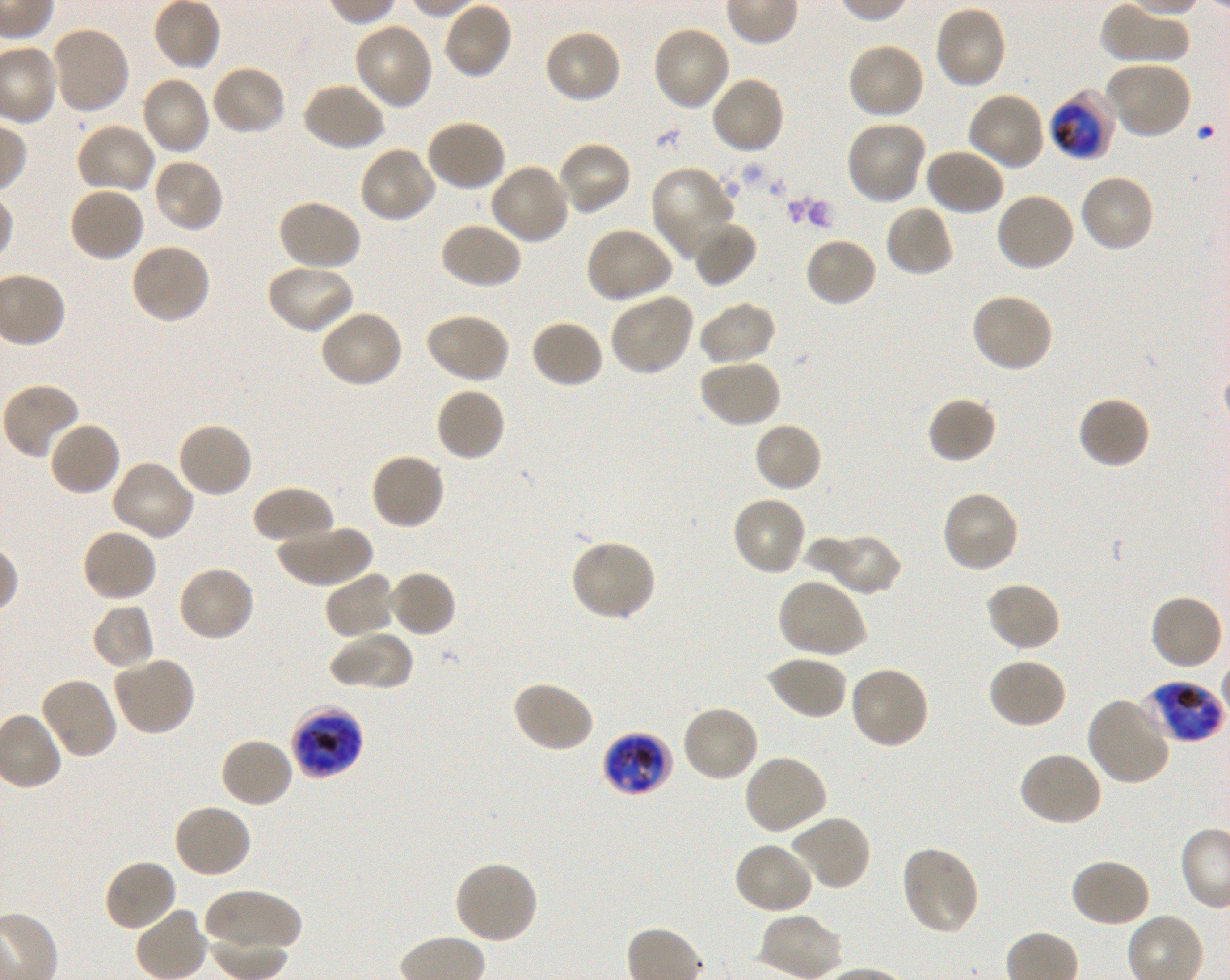 Approximate bounding rectangles given as corner coordinates in pixels from the top-left. Not every red blood cell is marked. A life-cycle stage — or a range of stages, where the recorded stages span more than one — follows each staged infected red blood cell. Locations of infected red blood cells: (x1=1049, y1=90, x2=1117, y2=160) early trophozoite to late schizont; (x1=1141, y1=681, x2=1224, y2=743) late trophozoite to early schizont; (x1=291, y1=704, x2=365, y2=779) late trophozoite to late schizont; (x1=602, y1=731, x2=673, y2=796) early trophozoite to early schizont. Locations of uninfected red blood cells: (x1=442, y1=1, x2=514, y2=81), (x1=1101, y1=1, x2=1190, y2=64), (x1=933, y1=5, x2=1007, y2=90), (x1=353, y1=22, x2=434, y2=110), (x1=651, y1=24, x2=730, y2=111), (x1=50, y1=25, x2=131, y2=115), (x1=543, y1=28, x2=623, y2=104), (x1=846, y1=42, x2=926, y2=120), (x1=1106, y1=61, x2=1193, y2=140), (x1=210, y1=64, x2=287, y2=137), (x1=139, y1=75, x2=211, y2=156), (x1=709, y1=75, x2=786, y2=155), (x1=302, y1=82, x2=386, y2=152), (x1=966, y1=91, x2=1045, y2=172), (x1=425, y1=118, x2=507, y2=193), (x1=845, y1=120, x2=927, y2=204), (x1=74, y1=122, x2=156, y2=195), (x1=557, y1=140, x2=632, y2=217), (x1=358, y1=145, x2=436, y2=224), (x1=923, y1=148, x2=1005, y2=217), (x1=152, y1=157, x2=225, y2=235), (x1=489, y1=163, x2=570, y2=245), (x1=650, y1=165, x2=737, y2=261), (x1=1077, y1=173, x2=1156, y2=254), (x1=68, y1=186, x2=146, y2=263), (x1=993, y1=190, x2=1075, y2=273), (x1=276, y1=199, x2=362, y2=273), (x1=885, y1=204, x2=955, y2=277), (x1=691, y1=220, x2=757, y2=287), (x1=439, y1=222, x2=522, y2=291), (x1=585, y1=227, x2=674, y2=304), (x1=804, y1=235, x2=878, y2=308), (x1=129, y1=242, x2=212, y2=325), (x1=265, y1=263, x2=355, y2=335), (x1=970, y1=292, x2=1055, y2=374), (x1=608, y1=293, x2=695, y2=377), (x1=698, y1=301, x2=777, y2=367), (x1=318, y1=308, x2=404, y2=389), (x1=423, y1=312, x2=511, y2=385), (x1=530, y1=319, x2=605, y2=389), (x1=697, y1=359, x2=781, y2=430), (x1=1, y1=382, x2=82, y2=460), (x1=434, y1=387, x2=506, y2=463), (x1=927, y1=395, x2=997, y2=465), (x1=1076, y1=395, x2=1151, y2=471), (x1=47, y1=420, x2=121, y2=497), (x1=753, y1=421, x2=824, y2=492), (x1=175, y1=422, x2=254, y2=499), (x1=369, y1=452, x2=446, y2=532), (x1=110, y1=461, x2=194, y2=543), (x1=252, y1=486, x2=335, y2=547), (x1=939, y1=490, x2=1020, y2=574), (x1=731, y1=494, x2=808, y2=576), (x1=274, y1=524, x2=373, y2=588), (x1=81, y1=528, x2=159, y2=603), (x1=824, y1=534, x2=903, y2=597), (x1=803, y1=536, x2=870, y2=591), (x1=569, y1=539, x2=656, y2=622), (x1=176, y1=563, x2=257, y2=642), (x1=387, y1=570, x2=457, y2=638), (x1=324, y1=571, x2=396, y2=641), (x1=776, y1=578, x2=868, y2=660), (x1=984, y1=582, x2=1062, y2=653), (x1=1149, y1=592, x2=1225, y2=671), (x1=91, y1=603, x2=156, y2=670), (x1=328, y1=630, x2=413, y2=691), (x1=112, y1=655, x2=196, y2=736), (x1=764, y1=655, x2=848, y2=722), (x1=986, y1=657, x2=1067, y2=730), (x1=848, y1=666, x2=929, y2=750), (x1=38, y1=676, x2=118, y2=760), (x1=510, y1=680, x2=594, y2=754), (x1=1086, y1=694, x2=1172, y2=786), (x1=679, y1=703, x2=760, y2=783), (x1=219, y1=737, x2=295, y2=809), (x1=1018, y1=751, x2=1104, y2=827), (x1=742, y1=754, x2=829, y2=836), (x1=171, y1=803, x2=253, y2=880), (x1=790, y1=815, x2=872, y2=892), (x1=733, y1=841, x2=815, y2=915), (x1=899, y1=845, x2=980, y2=935), (x1=104, y1=858, x2=178, y2=934), (x1=1069, y1=858, x2=1151, y2=929), (x1=452, y1=861, x2=539, y2=945), (x1=206, y1=889, x2=302, y2=954). Giemsa stain. P. falciparum strain 3D7 in shaking in-vitro culture. Thin blood film. Donor blood group O+. Image is 1230×980 pixels. One field from this slide. 100x objective under oil immersion, numerical aperture 1.30.